Report the malaria status of this cell.
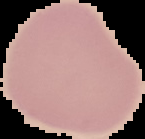

Uninfected.

image_type: segmented cell region on a black background
image_size: 145×139 pixels
preparation: thin blood smear